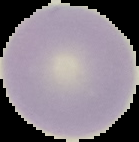
Summary:
  - Image type: segmented cell region on a black background
  - Preparation: thin blood smear
  - Image size: 139×142 pixels
  - Malaria status: uninfected